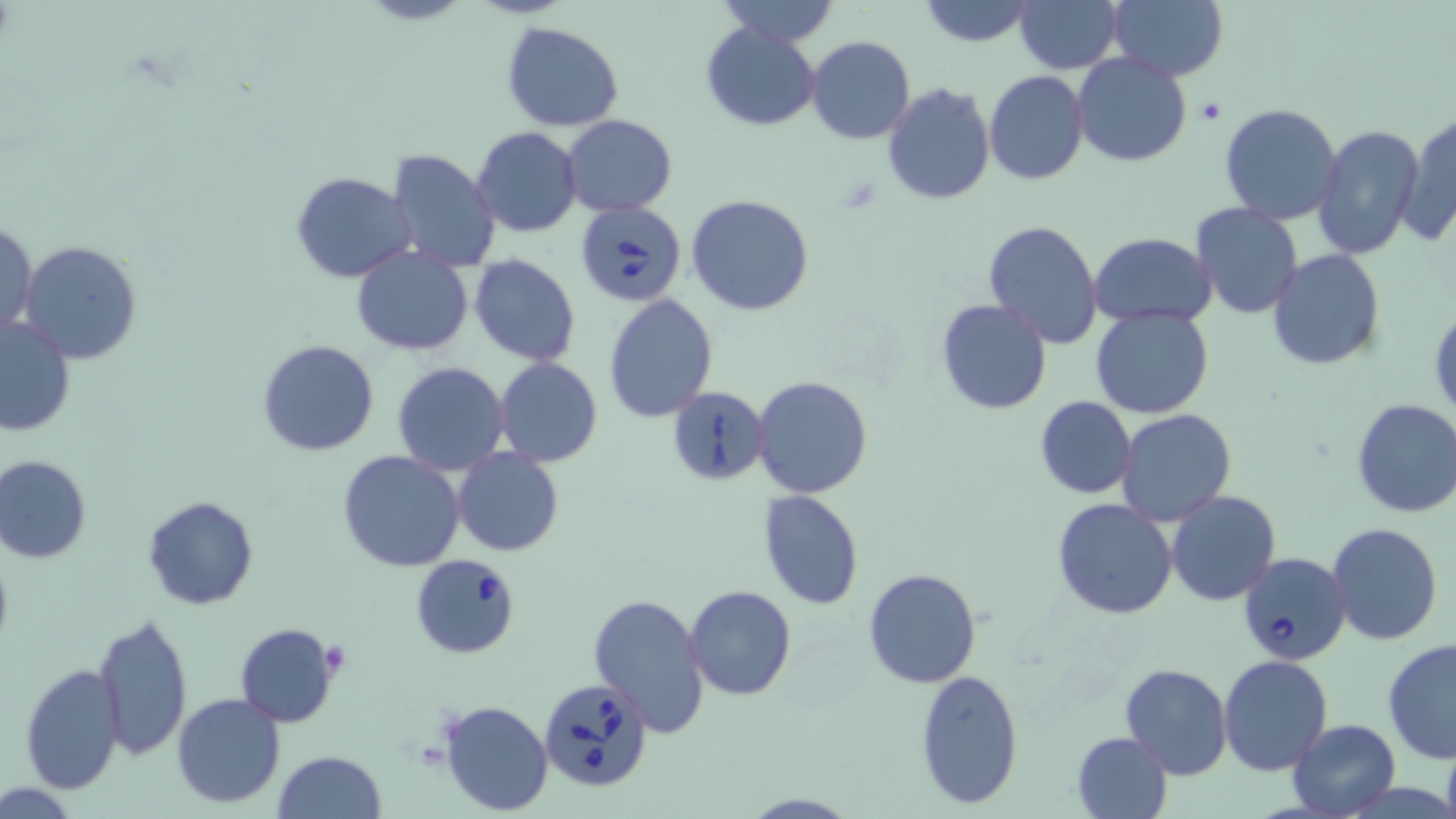
Approximate bounding boxes as (x1, y1, x2, y2) in pixels. Platelet locations: (1199, 100, 1226, 124). Uninfected red blood cell locations: (715, 0, 841, 47), (918, 0, 1038, 47), (1105, 0, 1230, 82), (1016, 1, 1121, 73), (502, 21, 626, 131), (700, 21, 821, 131), (806, 35, 915, 145), (1072, 53, 1192, 168), (984, 70, 1091, 185), (880, 83, 996, 205), (1219, 103, 1345, 225), (1399, 113, 1455, 246), (560, 114, 677, 217), (1313, 123, 1423, 259), (471, 127, 583, 237), (388, 148, 500, 275), (291, 171, 417, 282), (687, 194, 815, 315), (1191, 203, 1304, 319), (1, 218, 37, 340), (982, 219, 1103, 350), (1090, 233, 1216, 326), (18, 240, 145, 365), (351, 247, 474, 355), (1268, 249, 1384, 370), (468, 254, 581, 366), (604, 295, 717, 423), (936, 298, 1053, 416), (1090, 307, 1215, 420), (1428, 307, 1456, 422), (0, 314, 74, 438), (258, 339, 380, 456), (494, 357, 603, 467), (391, 361, 509, 476), (752, 375, 873, 499), (666, 385, 770, 485), (1034, 396, 1137, 499), (1350, 397, 1456, 520), (1116, 409, 1237, 527), (453, 449, 563, 557), (337, 450, 466, 572), (0, 454, 93, 563), (1167, 490, 1281, 606), (759, 491, 864, 609), (142, 496, 259, 610), (1051, 498, 1177, 621), (1326, 521, 1444, 646), (862, 568, 982, 689), (684, 585, 796, 701), (588, 591, 710, 736), (93, 614, 194, 761), (234, 623, 340, 727), (1383, 638, 1456, 765), (1219, 655, 1333, 775), (20, 663, 126, 797), (1119, 663, 1233, 780), (916, 670, 1023, 810), (171, 693, 286, 807), (439, 699, 553, 816), (1285, 718, 1400, 818), (1071, 732, 1173, 818), (272, 750, 386, 819). Babesia divergens-infected red blood cell locations: (577, 199, 684, 306), (1237, 549, 1351, 666), (410, 555, 521, 659), (538, 678, 653, 793). Slide-level diagnosis: Babesia divergens. Image is 1456×819 pixels. One field of a larger specimen. May-Grünwald-Giemsa stain. Thin blood film. Captured at 1000x magnification. Light microscopy.